Assess this cell for malaria.
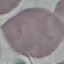
Uninfected.

Summary:
  - Capture: smartphone through the microscope eyepiece
  - Preparation: thin blood film
  - Image type: automatically extracted cell patch, resized to 64 × 64 pixels
  - Stain: Giemsa